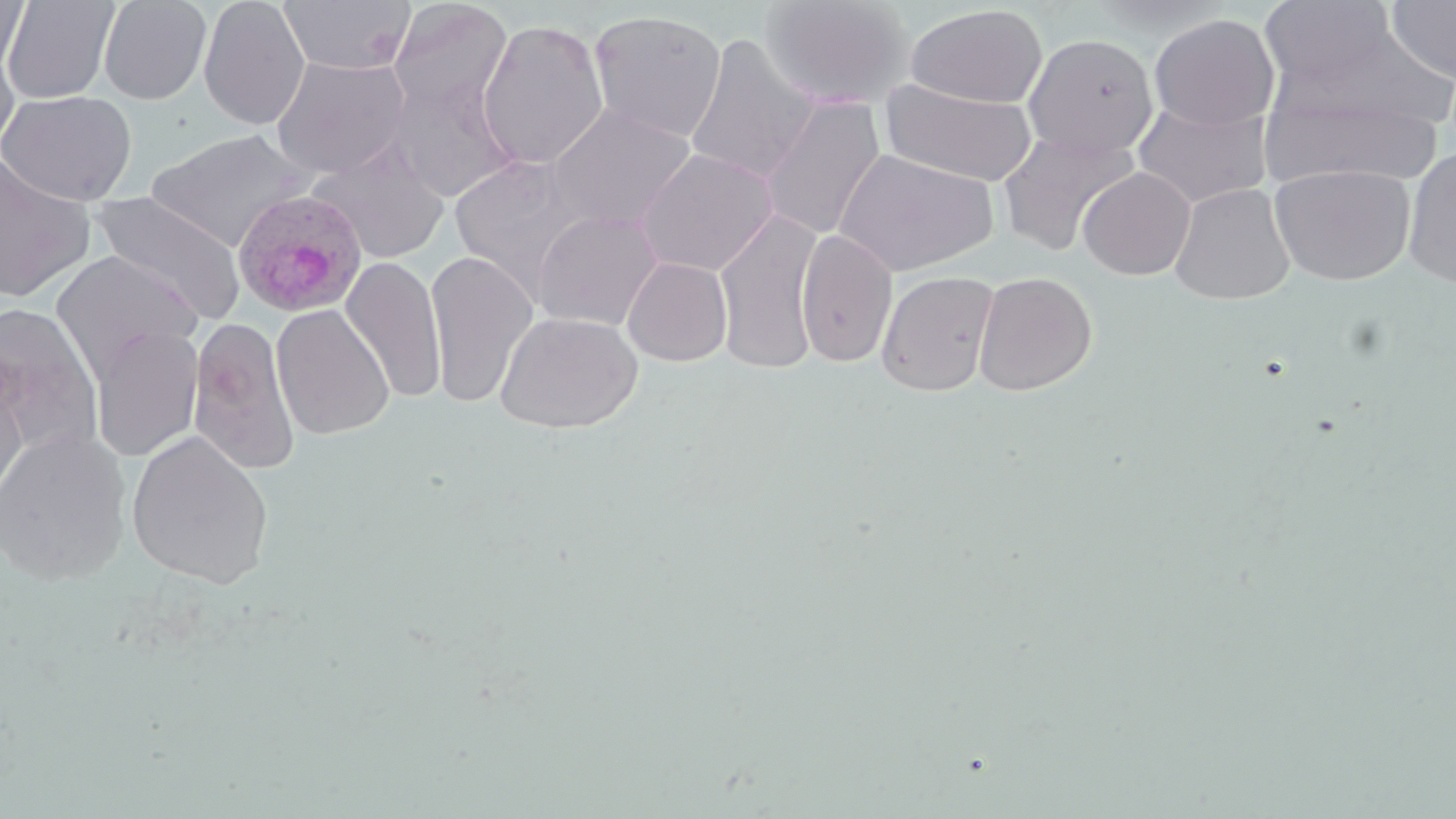 Approximate bounding boxes as (x1,y1)-(x2,y2) corner pairs in pixels. Plasmodium ovale-infected red blood cell locations: (231,188)-(367,317). Uninfected red blood cell locations: (0,0)-(31,78), (2,0)-(120,104), (198,0)-(310,130), (277,0)-(416,75), (759,0)-(913,110), (1259,0)-(1399,92), (1386,0)-(1456,86), (98,1)-(212,105), (387,1)-(512,118), (905,4)-(1048,109), (588,9)-(728,143), (1148,13)-(1280,130), (477,18)-(609,170), (0,19)-(23,150), (1023,33)-(1159,158), (684,34)-(820,186), (272,55)-(411,177), (387,72)-(521,203), (879,77)-(1039,188), (0,89)-(137,206), (1261,92)-(1445,189), (757,96)-(886,241), (1133,100)-(1272,209), (546,103)-(697,231), (997,128)-(1139,257), (145,129)-(310,252), (307,142)-(450,263), (636,147)-(778,277), (834,148)-(997,277), (1402,148)-(1456,289), (0,155)-(96,303), (449,156)-(594,293), (1270,164)-(1415,286), (1078,167)-(1196,280), (1170,183)-(1295,304), (90,191)-(246,325), (713,208)-(825,376), (531,209)-(664,331), (795,229)-(898,368), (51,250)-(202,381), (425,250)-(540,410), (341,255)-(447,404), (622,256)-(733,366), (876,270)-(1000,397), (972,271)-(1097,396), (0,302)-(105,462), (271,304)-(395,440), (495,311)-(642,434), (189,317)-(301,476), (91,325)-(204,463), (0,363)-(30,509), (0,428)-(132,587), (126,430)-(275,589). Slide-level diagnosis: Plasmodium ovale. Image is 1456×819 pixels. May-Grünwald-Giemsa stain. Thin blood smear. 1000x magnification. Single field of view. Light microscopy.